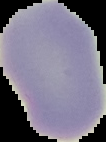
result = negative for malaria parasites
image size = 106×142 pixels
preparation = thin blood smear
image type = cell region segmented out of the field of view; surrounding area masked to black